Identify the cell.
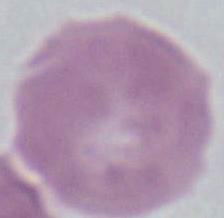

This is an erythrocyte.

Photomicrograph. Captured at 1000x magnification.